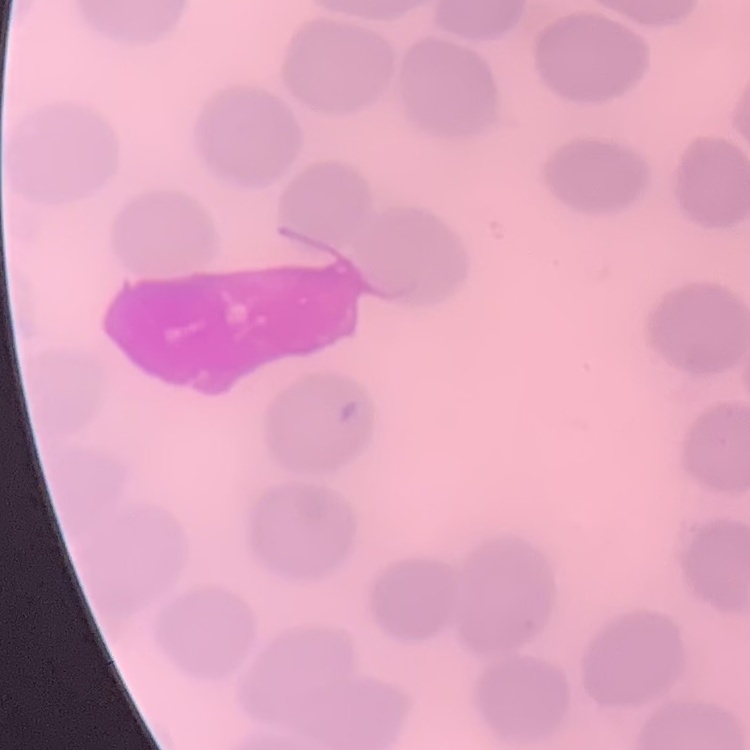
Summary:
  - Red blood cell morphology: no rouleaux formation
  - Image type: one tile cut from a larger photomicrograph
  - Stain: Field's or Giemsa
  - Preparation: thin peripheral smear